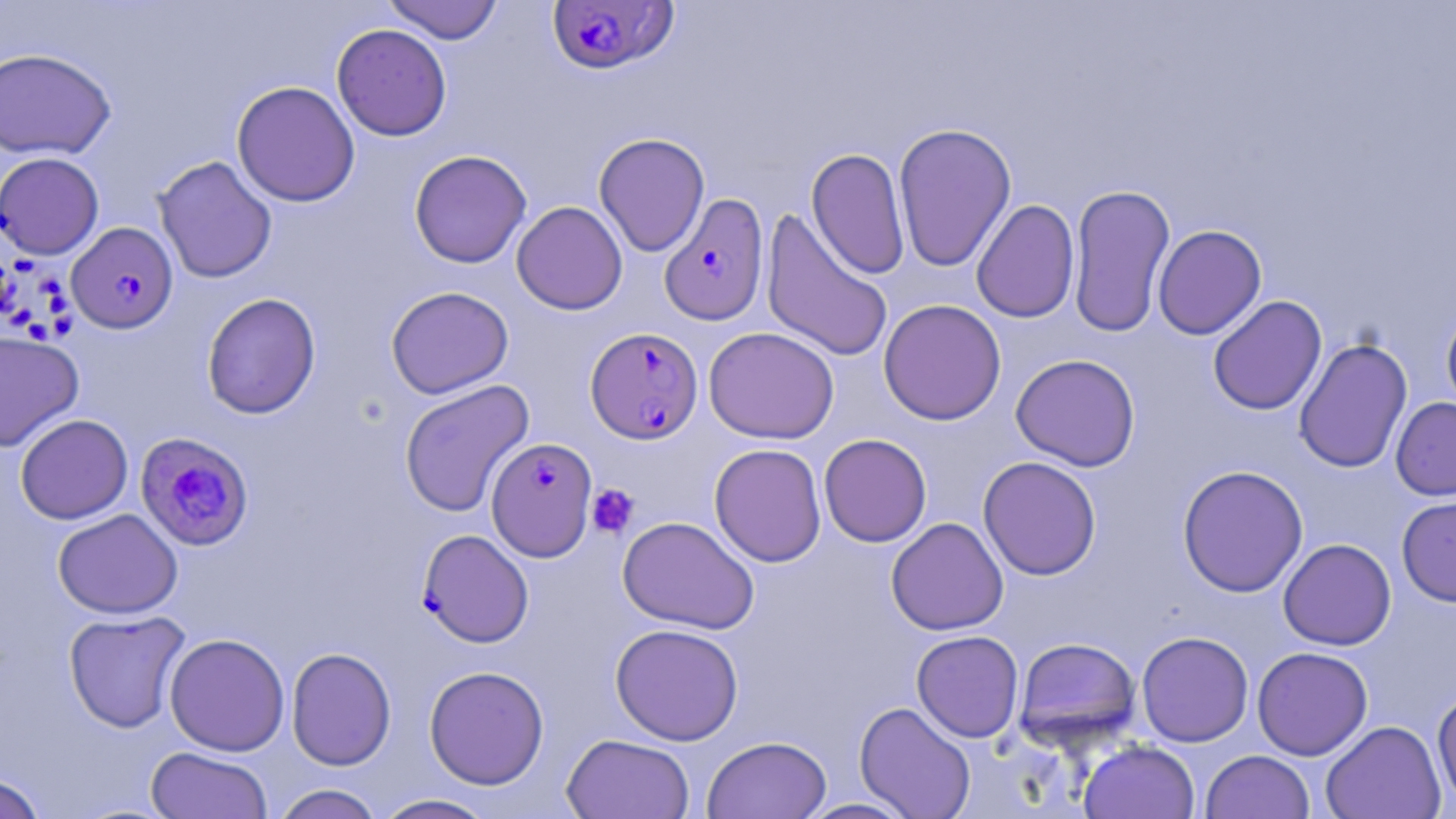

slide_level_diagnosis: Plasmodium falciparum
uninfected_red_blood_cell_locations: 'approximate bounding boxes as named x1/y1/x2/y2 corners in pixels: (x1=382, y1=0, x2=504, y2=44), (x1=331, y1=23, x2=452, y2=141), (x1=0, y1=47, x2=116, y2=160), (x1=231, y1=80, x2=360, y2=207), (x1=893, y1=122, x2=1017, y2=272), (x1=593, y1=132, x2=710, y2=257), (x1=806, y1=147, x2=911, y2=280), (x1=409, y1=149, x2=531, y2=268), (x1=0, y1=152, x2=104, y2=259), (x1=153, y1=155, x2=277, y2=283), (x1=1067, y1=183, x2=1175, y2=337), (x1=971, y1=199, x2=1080, y2=323), (x1=511, y1=201, x2=628, y2=315), (x1=760, y1=208, x2=894, y2=364), (x1=1152, y1=224, x2=1266, y2=340), (x1=385, y1=285, x2=514, y2=399), (x1=201, y1=292, x2=321, y2=419), (x1=1208, y1=295, x2=1327, y2=415), (x1=878, y1=298, x2=1006, y2=426), (x1=1441, y1=304, x2=1456, y2=418), (x1=703, y1=326, x2=839, y2=444), (x1=0, y1=331, x2=85, y2=451), (x1=1294, y1=337, x2=1413, y2=473), (x1=1010, y1=353, x2=1141, y2=471), (x1=399, y1=379, x2=535, y2=517), (x1=1390, y1=396, x2=1456, y2=501), (x1=15, y1=413, x2=133, y2=524), (x1=818, y1=433, x2=932, y2=547), (x1=709, y1=443, x2=827, y2=567), (x1=978, y1=456, x2=1102, y2=580), (x1=1177, y1=464, x2=1308, y2=598), (x1=1396, y1=494, x2=1456, y2=607), (x1=52, y1=508, x2=183, y2=619), (x1=617, y1=516, x2=760, y2=634), (x1=886, y1=517, x2=1008, y2=635), (x1=1278, y1=538, x2=1396, y2=650), (x1=63, y1=610, x2=191, y2=733), (x1=610, y1=623, x2=744, y2=745), (x1=911, y1=630, x2=1024, y2=742), (x1=1136, y1=631, x2=1254, y2=747), (x1=164, y1=632, x2=290, y2=756), (x1=1013, y1=636, x2=1141, y2=750), (x1=1252, y1=646, x2=1373, y2=760), (x1=286, y1=647, x2=396, y2=770), (x1=423, y1=665, x2=549, y2=789), (x1=1432, y1=687, x2=1456, y2=811), (x1=854, y1=702, x2=976, y2=819), (x1=1321, y1=720, x2=1446, y2=819), (x1=561, y1=733, x2=696, y2=819), (x1=702, y1=735, x2=831, y2=819), (x1=1078, y1=740, x2=1200, y2=819), (x1=145, y1=746, x2=273, y2=818), (x1=1201, y1=750, x2=1315, y2=819), (x1=1, y1=772, x2=48, y2=819), (x1=271, y1=784, x2=385, y2=819), (x1=373, y1=794, x2=499, y2=819), (x1=797, y1=798, x2=919, y2=818)'
plasmodium_falciparum_infected_red_blood_cell_locations: 'approximate bounding boxes as named x1/y1/x2/y2 corners in pixels: (x1=548, y1=1, x2=680, y2=76), (x1=659, y1=192, x2=769, y2=327), (x1=66, y1=222, x2=178, y2=335), (x1=585, y1=327, x2=703, y2=444), (x1=135, y1=431, x2=254, y2=551), (x1=486, y1=437, x2=598, y2=561), (x1=418, y1=529, x2=534, y2=647)'
magnification: 1000x
preparation: thin blood smear
modality: optical microscopy
image_size: 1456×819 pixels
platelet_locations: 'approximate bounding boxes as named x1/y1/x2/y2 corners in pixels: (x1=586, y1=483, x2=640, y2=538)'
stain: May-Grünwald-Giemsa
field_of_view: one of a larger specimen